Comment on the morphology of the erythrocytes.
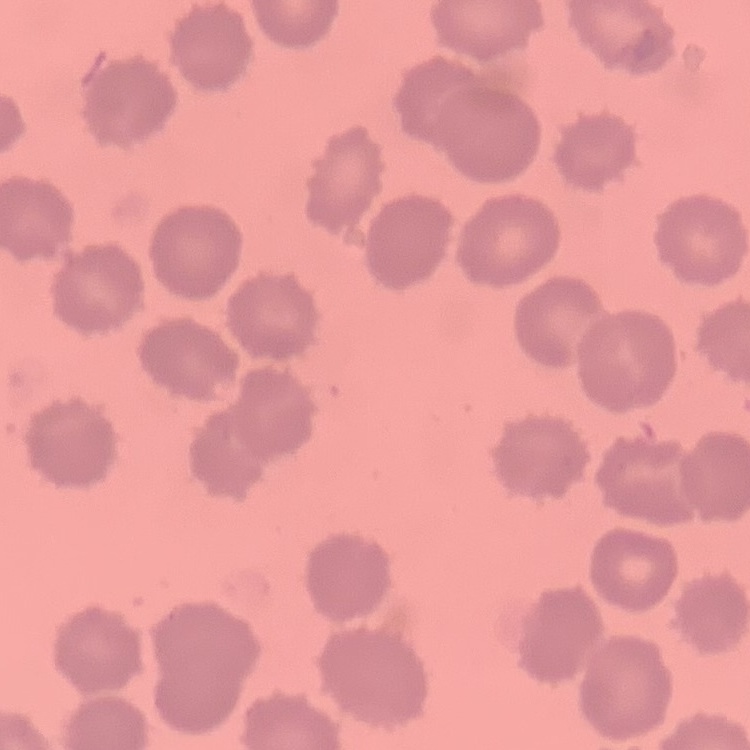
No rouleaux formation.

One tile cut from a larger photomicrograph. Field's or Giemsa stain. Thin blood film.